Point out each leukocyte.
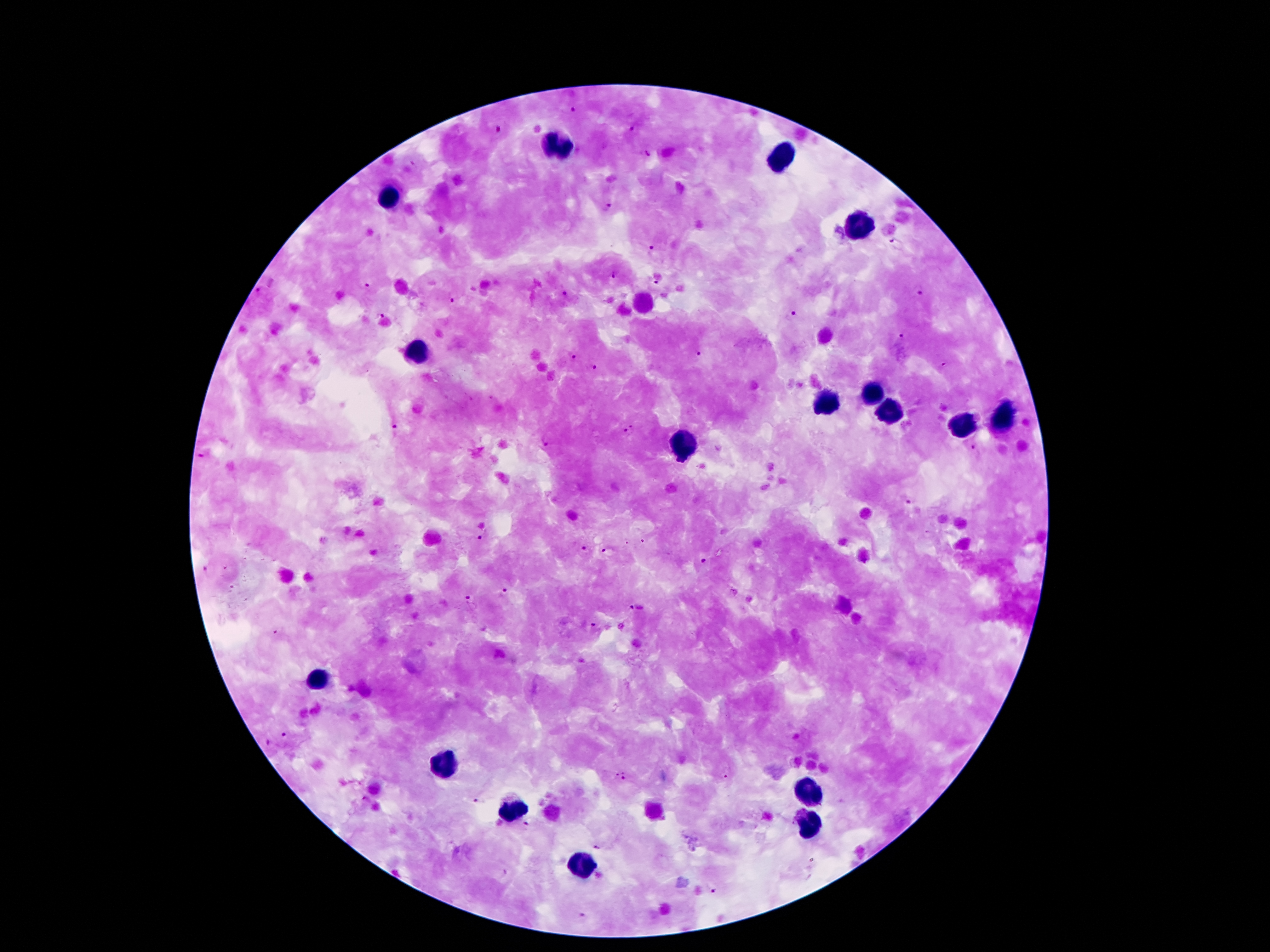

Approximate centers as (x, y) in pixels.
Leukocytes: (555, 147), (779, 155), (391, 197), (859, 229), (419, 349), (873, 393), (823, 403), (889, 410), (1001, 421), (963, 428), (685, 445), (319, 680), (445, 768), (805, 793), (511, 813), (809, 828), (577, 866).

Summary:
  - Malaria parasite locations: (573, 109), (498, 129), (633, 129), (648, 155), (414, 164), (607, 207), (898, 243), (651, 248), (614, 274), (656, 280), (367, 286), (918, 288), (261, 291), (563, 293), (450, 294), (380, 315), (791, 316), (900, 337), (698, 354), (570, 356), (946, 366), (591, 368), (631, 429), (395, 430), (546, 443), (974, 449), (198, 458), (913, 502), (479, 536), (583, 548), (604, 551), (705, 563), (205, 569), (503, 590), (468, 601), (635, 608), (590, 629), (277, 630), (287, 733), (269, 744), (621, 778), (480, 803), (526, 826), (597, 847), (714, 891), (584, 917)
  - Image size: 1270×952 pixels
  - Patient malaria status: positive for Plasmodium falciparum
  - Field of view: single
  - Stain: Giemsa
  - Preparation: thick peripheral-blood smear
  - Magnification: 100x
  - Capture: smartphone through the microscope eyepiece